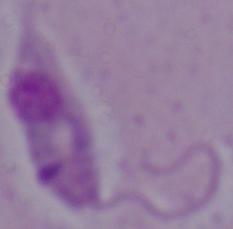

Captured at 1000x magnification. A Leishmania parasite is seen. Photomicrograph.